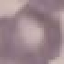
result = no malaria parasites detected
preparation = thin smear
image type = automatically extracted cell patch, resized to 64 × 64 pixels
stain = Giemsa
capture = smartphone through the microscope eyepiece